Identify the parasite.
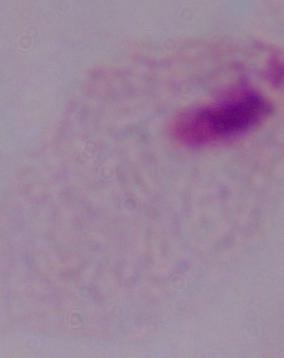

A trichomonad.

Summary:
  - Modality: photomicrograph
  - Magnification: 1000x